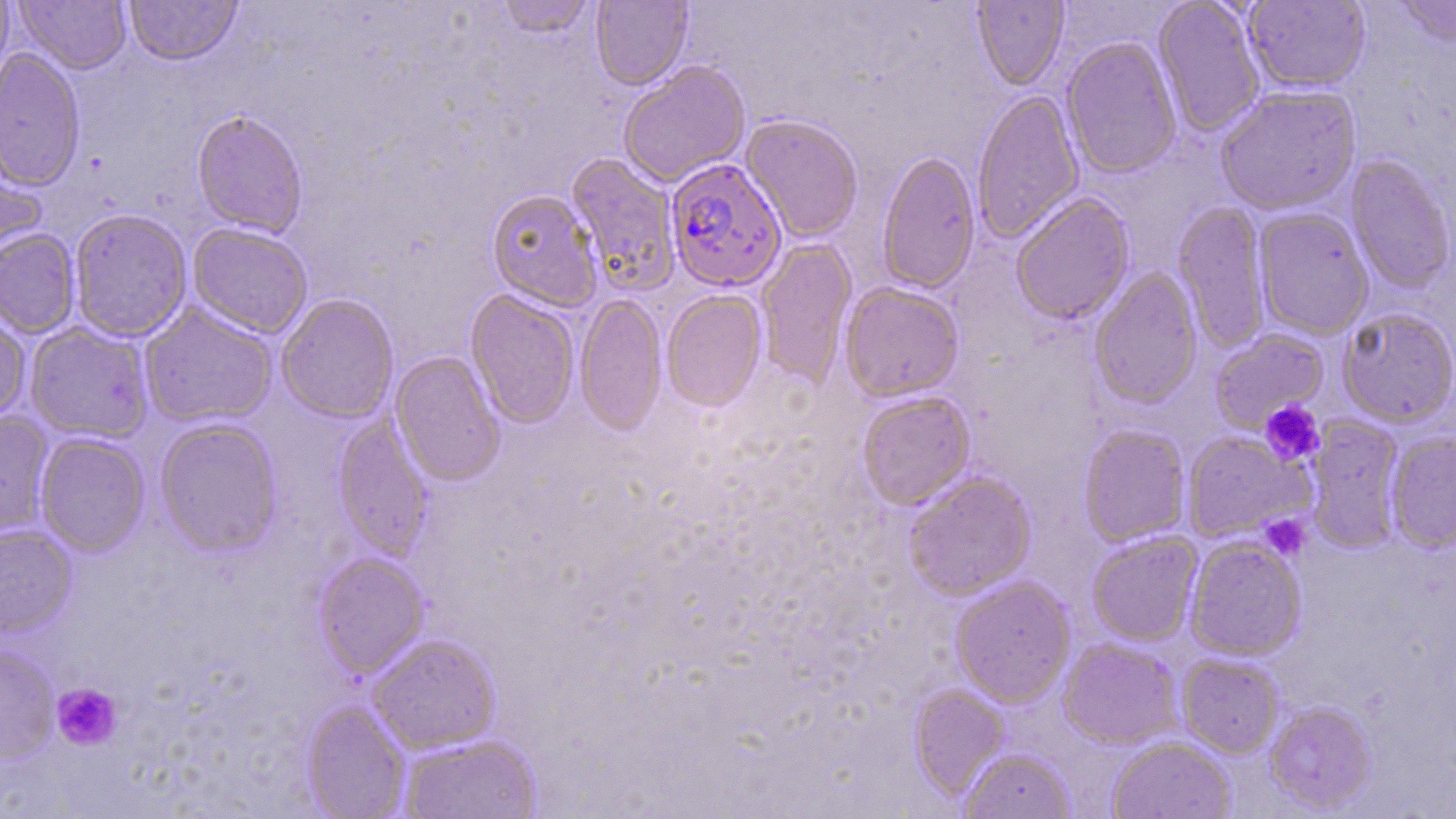

Approximate bounding boxes as (x1, y1, x2, y2) in pixels. Platelet locations: (1258, 399, 1325, 467), (1260, 514, 1310, 560), (51, 683, 122, 751). Uninfected red blood cell locations: (0, 0, 13, 84), (124, 0, 243, 68), (496, 0, 596, 39), (972, 0, 1069, 91), (1152, 0, 1266, 138), (1393, 0, 1456, 49), (14, 1, 131, 75), (591, 1, 693, 91), (1243, 1, 1371, 94), (1062, 37, 1182, 179), (0, 49, 85, 192), (618, 60, 751, 188), (1216, 85, 1361, 216), (972, 90, 1085, 244), (191, 112, 308, 239), (740, 115, 863, 243), (0, 146, 47, 273), (877, 150, 981, 295), (566, 153, 681, 296), (1345, 155, 1455, 294), (487, 191, 603, 312), (1010, 192, 1135, 326), (1173, 202, 1271, 353), (1253, 208, 1374, 340), (69, 209, 193, 343), (187, 223, 313, 339), (0, 229, 80, 338), (756, 239, 857, 390), (1089, 267, 1203, 410), (840, 282, 964, 402), (465, 290, 580, 430), (662, 290, 767, 412), (276, 294, 399, 424), (575, 294, 667, 437), (139, 303, 278, 428), (0, 307, 32, 423), (1338, 308, 1456, 428), (25, 323, 154, 443), (1209, 328, 1329, 433), (389, 351, 506, 488), (856, 391, 975, 511), (0, 411, 54, 538), (332, 413, 434, 561), (1305, 415, 1406, 554), (155, 419, 283, 558), (1078, 424, 1191, 547), (1385, 431, 1456, 552), (1182, 432, 1310, 543), (35, 433, 150, 557), (903, 471, 1038, 600), (0, 524, 78, 637), (1086, 532, 1203, 647), (1184, 536, 1306, 661), (312, 552, 429, 680), (950, 576, 1076, 707), (367, 635, 502, 754), (1058, 638, 1184, 750), (0, 645, 59, 765), (1177, 654, 1284, 758), (909, 685, 1009, 800), (301, 701, 411, 819), (1265, 701, 1377, 813), (398, 734, 542, 819), (1106, 736, 1236, 819), (959, 748, 1075, 819). Plasmodium falciparum-infected red blood cell locations: (666, 159, 787, 293). Slide-level diagnosis: Plasmodium falciparum. May-Grünwald-Giemsa stain. Image is 1456×819 pixels. One field of a larger specimen. Thin blood smear. 1000x magnification. Light microscopy.